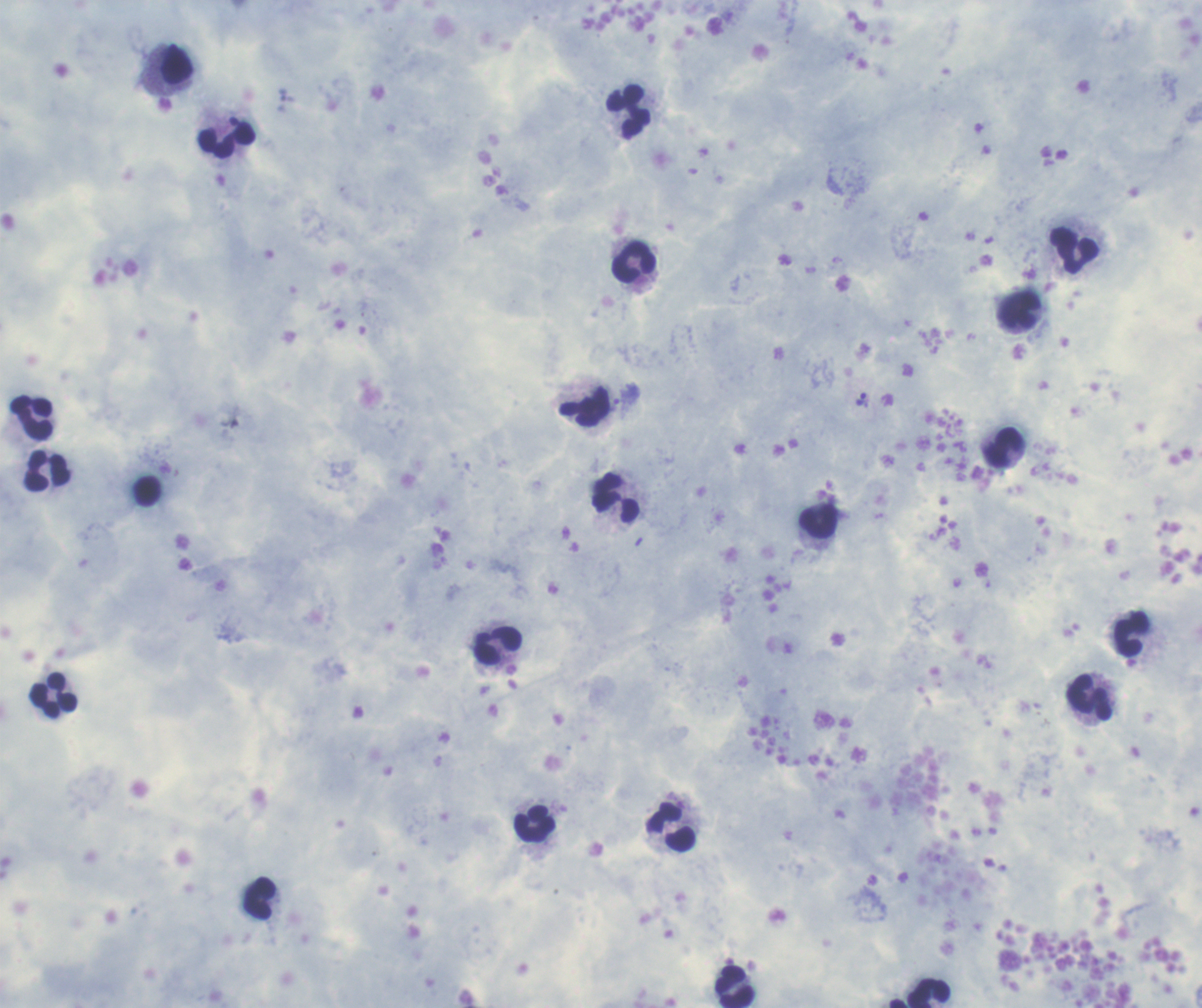 Coloration quality: good. Image is 1202×1008 pixels. Thick blood film. Single field of view. Romanowsky-stained preparation.